Outline each blood parasite and name the species.
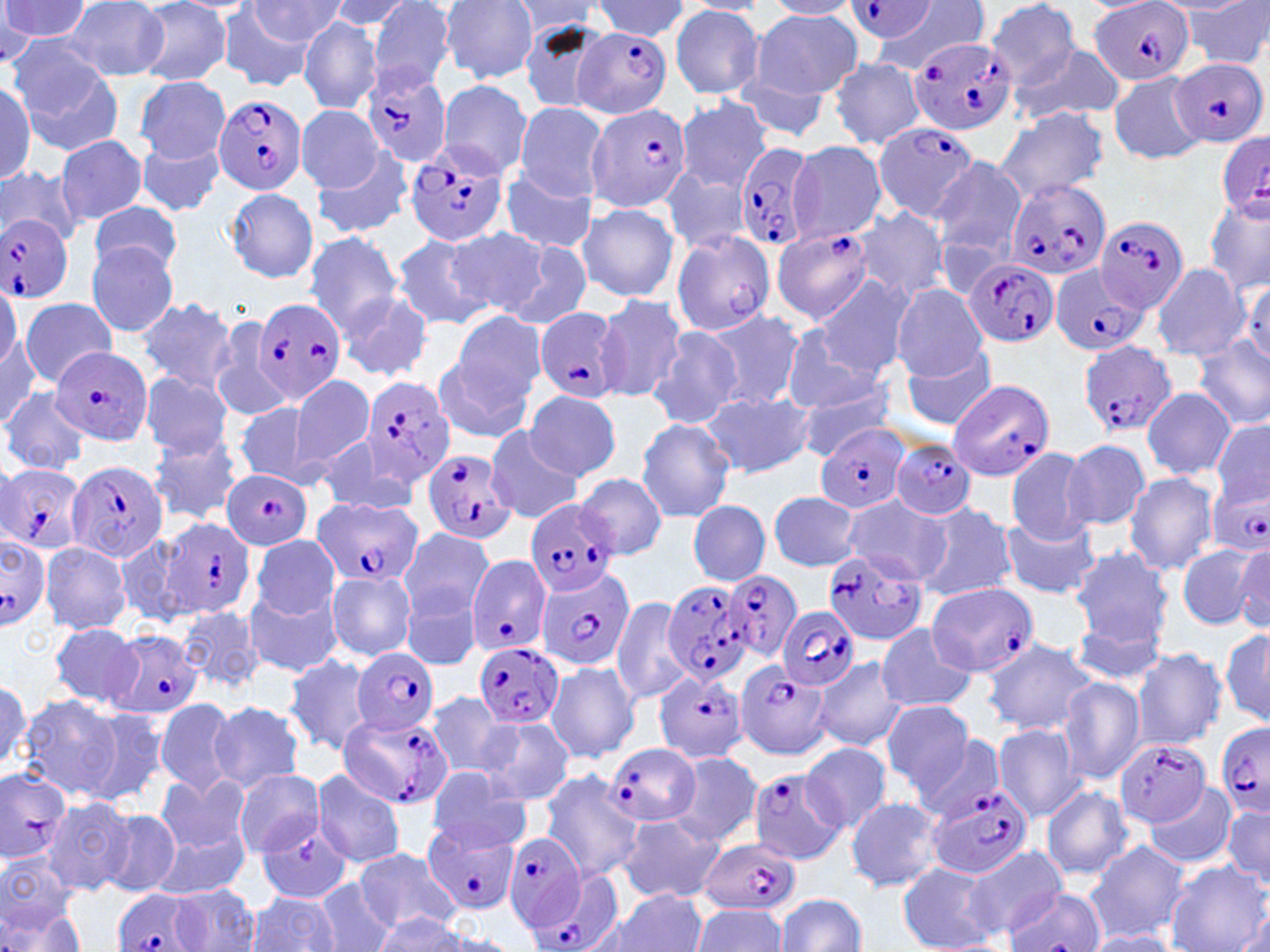

Approximate bounding boxes as (x1,y1)-(x2,y2) corner pairs in pixels.
Plasmodium falciparum-infected red blood cells: (1089,0)-(1195,86), (843,2)-(939,44), (573,25)-(673,119), (906,35)-(1017,137), (1170,57)-(1266,149), (360,69)-(453,168), (214,95)-(307,195), (589,103)-(693,213), (873,122)-(981,223), (1214,131)-(1270,223), (733,139)-(821,255), (405,143)-(506,247), (1002,179)-(1109,281), (0,214)-(74,301), (1094,215)-(1189,314), (771,226)-(872,324), (669,228)-(775,336), (963,258)-(1058,349), (1047,264)-(1152,356), (254,298)-(347,403), (535,306)-(629,402), (1078,340)-(1178,439), (52,347)-(152,446), (357,375)-(457,487), (947,377)-(1055,483), (817,422)-(911,516), (891,439)-(977,520), (422,448)-(513,545), (69,460)-(168,564), (0,464)-(87,554), (221,469)-(311,550), (1208,475)-(1268,561), (312,497)-(425,590), (529,500)-(621,597), (157,517)-(256,619), (0,535)-(51,630), (821,547)-(931,644), (465,555)-(553,657), (537,566)-(635,672), (723,569)-(803,663), (660,576)-(754,688), (924,582)-(1039,677), (777,606)-(862,691), (105,630)-(204,719), (476,642)-(564,728), (352,646)-(438,737), (737,661)-(835,758), (656,673)-(747,764), (337,711)-(455,813), (1216,720)-(1270,822), (1113,736)-(1210,829), (603,741)-(699,828), (746,770)-(847,865), (926,785)-(1032,879), (422,817)-(520,914), (502,833)-(588,931), (699,836)-(801,917), (525,872)-(625,952), (1004,887)-(1109,952), (112,888)-(205,952).
No Plasmodium ovale, Plasmodium malariae, Plasmodium vivax, Babesia divergens, or Trypanosoma brucei observed.

Summary:
  - Uninfected red blood cell locations: (0,0)-(93,49), (327,0)-(421,33), (985,0)-(1083,87), (245,1)-(348,45), (366,1)-(455,95), (440,1)-(539,84), (592,1)-(690,40), (765,1)-(863,19), (61,2)-(170,80), (134,2)-(233,85), (509,2)-(603,35), (873,2)-(989,71), (1183,3)-(1270,69), (670,5)-(765,98), (217,7)-(322,90), (750,11)-(862,100), (298,16)-(382,115), (518,19)-(612,114), (10,44)-(125,156), (1011,44)-(1121,122), (828,57)-(925,149), (1108,70)-(1207,164), (727,75)-(832,143), (136,76)-(229,161), (437,80)-(534,178), (0,81)-(35,188), (675,97)-(771,194), (514,102)-(607,200), (296,105)-(383,191), (994,107)-(1109,205), (135,132)-(226,217), (56,135)-(147,225), (789,142)-(887,244), (309,148)-(414,241), (928,157)-(1026,263), (0,166)-(82,246), (500,166)-(598,254), (661,167)-(750,255), (227,188)-(319,282), (1203,195)-(1270,296), (89,200)-(184,279), (575,203)-(679,302), (852,207)-(953,305), (445,225)-(548,320), (303,231)-(405,334), (391,234)-(491,331), (501,241)-(594,333), (87,242)-(179,336), (1150,262)-(1250,362), (1239,276)-(1270,370), (817,277)-(913,378), (0,282)-(21,375), (890,284)-(988,380), (338,289)-(432,381), (597,294)-(687,402), (20,297)-(115,386), (135,297)-(237,395), (704,309)-(803,410), (453,313)-(548,412), (209,317)-(290,422), (649,326)-(741,430), (781,328)-(887,418), (0,332)-(42,429), (1192,337)-(1270,431), (899,346)-(999,431), (433,356)-(534,445), (289,373)-(375,473), (141,374)-(233,458), (794,384)-(902,460), (1141,387)-(1237,480), (0,388)-(90,477), (523,389)-(620,482), (702,391)-(813,477), (234,403)-(318,488), (636,417)-(737,522), (1210,418)-(1269,510), (482,427)-(582,523), (147,432)-(244,525), (316,435)-(416,518), (1063,440)-(1149,532), (1006,446)-(1100,544), (1123,471)-(1220,575), (576,472)-(668,561), (768,490)-(862,572), (841,495)-(949,584), (914,501)-(1017,603), (689,502)-(771,584), (999,512)-(1102,600), (397,527)-(495,625), (251,535)-(340,619), (1188,540)-(1270,632), (39,541)-(132,634), (1232,544)-(1269,630), (1068,546)-(1173,650), (327,571)-(416,659), (246,583)-(343,678), (400,584)-(483,670), (610,596)-(695,706), (179,605)-(263,691), (1070,618)-(1171,687), (49,622)-(143,710), (875,624)-(977,713), (1219,624)-(1269,730), (980,636)-(1098,736), (1132,649)-(1228,749), (283,655)-(376,758), (813,656)-(907,751), (546,661)-(640,763), (1057,677)-(1145,783), (0,678)-(31,778), (423,692)-(512,778), (17,695)-(127,804), (154,696)-(240,797), (209,699)-(305,793), (879,699)-(976,797), (76,707)-(169,805), (478,718)-(574,806), (992,723)-(1086,821), (914,733)-(1008,823), (798,742)-(893,832), (669,751)-(764,848), (0,767)-(72,863), (233,769)-(324,857), (427,769)-(531,852), (311,770)-(407,868), (540,772)-(644,881), (156,773)-(249,855), (1144,784)-(1237,870), (1041,786)-(1133,881), (42,796)-(132,896), (845,796)-(945,893), (1221,803)-(1270,891), (98,809)-(182,898), (619,813)-(725,904), (255,822)-(352,903), (149,831)-(250,898), (1086,841)-(1190,944), (956,845)-(1068,939), (354,847)-(461,937), (0,853)-(79,936), (1165,862)-(1268,952), (899,864)-(997,951), (314,880)-(393,952), (170,884)-(260,951), (604,889)-(709,952), (244,892)-(342,951), (777,894)-(867,951), (2,897)-(88,952), (692,903)-(790,952), (1235,909)-(1268,952), (373,910)-(472,951), (1081,931)-(1180,952)
  - Slide-level diagnosis: Plasmodium falciparum
  - Magnification: 1000x
  - Image size: 1270×952 pixels
  - Modality: light microscopy
  - Stain: May-Grünwald-Giemsa
  - Preparation: thin blood smear
  - Field of view: single